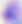
identification = Toxoplasma gondii
magnification = 400x
modality = micrograph